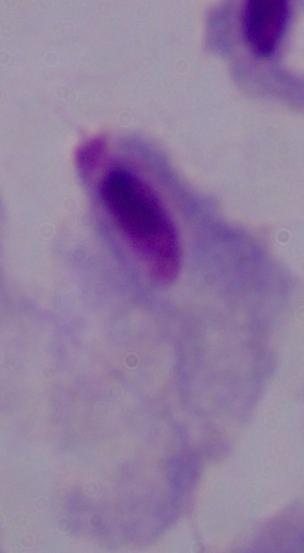
identification = trichomonad
modality = photomicrograph
magnification = 1000x